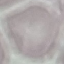
Summary:
  - Result: negative for malaria parasites
  - Preparation: thin smear
  - Stain: Giemsa
  - Capture: smartphone camera at the microscope eyepiece
  - Image type: cell patch, automatically extracted from a larger field of view and resized to 64 × 64 pixels